Identify the cell.
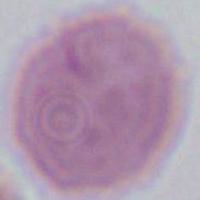
An erythrocyte.

Summary:
  - Modality: micrograph
  - Magnification: 1000x